Identify the parasite.
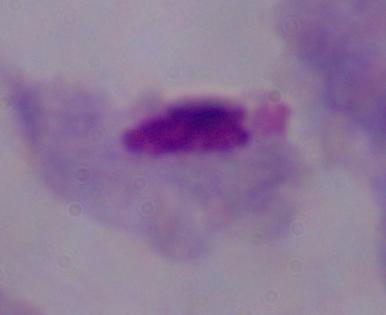
A trichomonad.

1000x magnification. Micrograph.